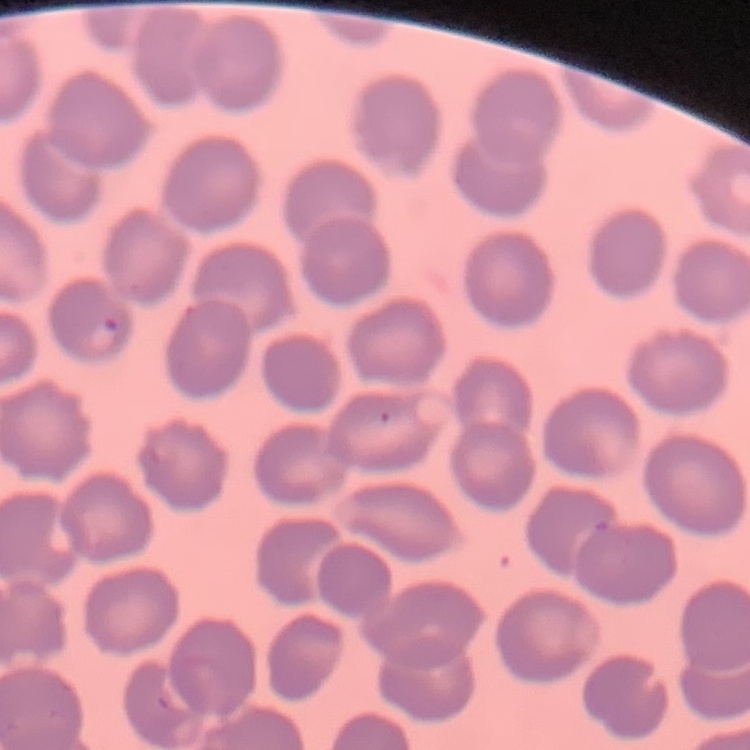
erythrocyte morphology = no rouleaux formation
stain = Field's or Giemsa
preparation = thin peripheral smear
image type = one tile cut from a larger photomicrograph